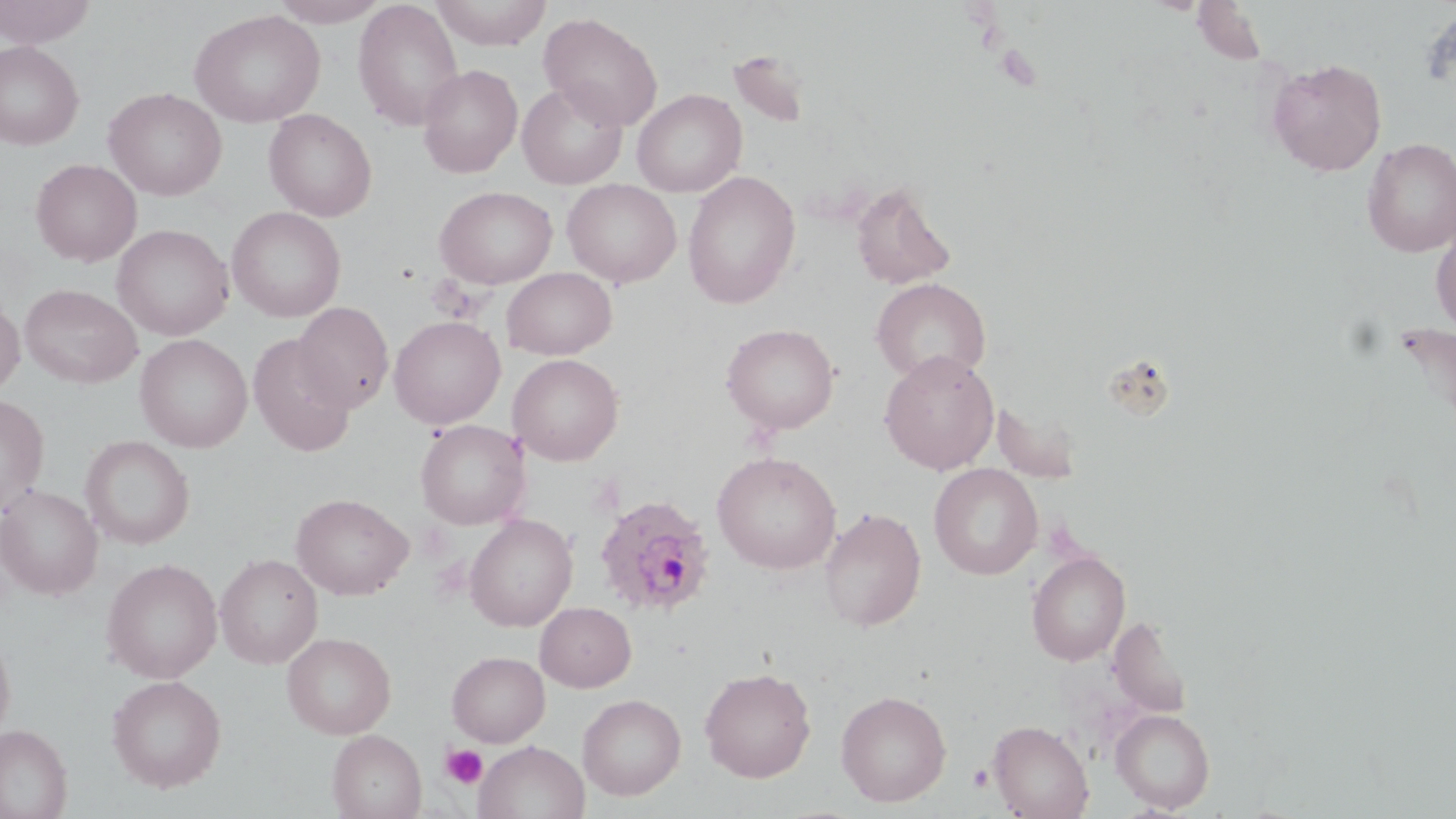
slide_level_diagnosis: Plasmodium ovale
preparation: thin blood film
plasmodium_ovale_infected_red_blood_cell_locations: 'approximate bounding boxes as named x1/y1/x2/y2 corners in pixels: (x1=593, y1=494, x2=717, y2=618)'
uninfected_red_blood_cell_locations: 'approximate bounding boxes as named x1/y1/x2/y2 corners in pixels: (x1=0, y1=0, x2=97, y2=47), (x1=267, y1=0, x2=391, y2=26), (x1=430, y1=0, x2=552, y2=49), (x1=352, y1=1, x2=464, y2=130), (x1=1193, y1=3, x2=1268, y2=65), (x1=188, y1=9, x2=325, y2=128), (x1=539, y1=13, x2=663, y2=131), (x1=0, y1=41, x2=84, y2=150), (x1=727, y1=49, x2=811, y2=129), (x1=1266, y1=58, x2=1387, y2=176), (x1=418, y1=64, x2=523, y2=178), (x1=517, y1=81, x2=628, y2=189), (x1=103, y1=87, x2=227, y2=201), (x1=632, y1=89, x2=746, y2=197), (x1=263, y1=109, x2=377, y2=221), (x1=1361, y1=138, x2=1456, y2=257), (x1=30, y1=159, x2=141, y2=267), (x1=683, y1=170, x2=800, y2=309), (x1=563, y1=179, x2=682, y2=287), (x1=850, y1=181, x2=956, y2=291), (x1=435, y1=185, x2=558, y2=289), (x1=227, y1=207, x2=346, y2=322), (x1=1431, y1=221, x2=1456, y2=339), (x1=112, y1=224, x2=234, y2=341), (x1=502, y1=267, x2=617, y2=359), (x1=871, y1=278, x2=991, y2=385), (x1=20, y1=284, x2=142, y2=388), (x1=0, y1=296, x2=25, y2=396), (x1=293, y1=302, x2=394, y2=412), (x1=389, y1=316, x2=505, y2=429), (x1=1393, y1=322, x2=1456, y2=448), (x1=721, y1=323, x2=840, y2=434), (x1=248, y1=334, x2=357, y2=456), (x1=135, y1=335, x2=252, y2=452), (x1=880, y1=350, x2=999, y2=475), (x1=508, y1=353, x2=624, y2=465), (x1=0, y1=394, x2=49, y2=515), (x1=992, y1=398, x2=1083, y2=484), (x1=415, y1=420, x2=530, y2=530), (x1=80, y1=435, x2=195, y2=550), (x1=712, y1=451, x2=841, y2=574), (x1=929, y1=463, x2=1043, y2=580), (x1=0, y1=485, x2=103, y2=599), (x1=291, y1=493, x2=413, y2=600), (x1=819, y1=508, x2=926, y2=632), (x1=465, y1=514, x2=578, y2=631), (x1=1027, y1=550, x2=1130, y2=666), (x1=215, y1=554, x2=323, y2=668), (x1=101, y1=558, x2=222, y2=683), (x1=535, y1=601, x2=636, y2=692), (x1=1109, y1=614, x2=1193, y2=719), (x1=0, y1=628, x2=16, y2=743), (x1=282, y1=632, x2=396, y2=739), (x1=446, y1=651, x2=549, y2=747), (x1=699, y1=666, x2=816, y2=782), (x1=107, y1=674, x2=227, y2=792), (x1=836, y1=690, x2=952, y2=807), (x1=577, y1=694, x2=686, y2=800), (x1=1111, y1=709, x2=1215, y2=812), (x1=988, y1=720, x2=1093, y2=818), (x1=0, y1=725, x2=72, y2=818), (x1=327, y1=729, x2=426, y2=819), (x1=474, y1=740, x2=589, y2=819)'
magnification: 1000x
stain: May-Grünwald-Giemsa
modality: optical microscopy
field_of_view: single
image_size: 1456×819 pixels
platelet_locations: 'approximate bounding boxes as named x1/y1/x2/y2 corners in pixels: (x1=442, y1=743, x2=488, y2=788), (x1=968, y1=764, x2=994, y2=791)'